Locate every Plasmodium falciparum-infected red blood cell.
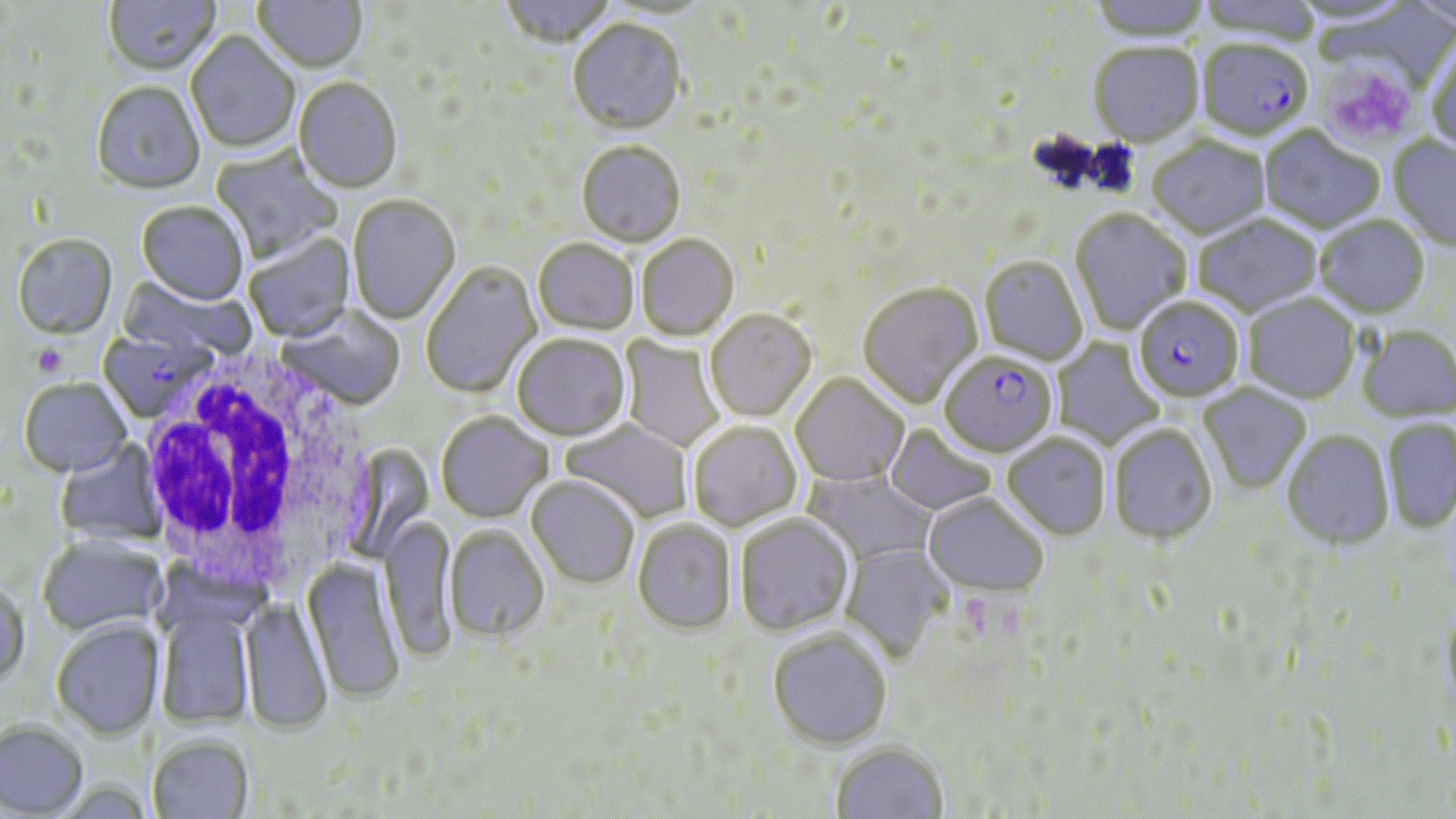

Approximate bounding boxes as [x1, y1, x2, y2] in pixels.
Plasmodium falciparum-infected red blood cells: [1196, 43, 1313, 145], [1133, 299, 1244, 405], [98, 329, 213, 423], [939, 354, 1057, 460].

White blood cell locations: [133, 354, 372, 595]. Platelet locations: [1324, 59, 1422, 158], [32, 346, 66, 377]. Uninfected red blood cell locations: [104, 0, 220, 78], [253, 0, 367, 75], [499, 0, 615, 51], [1086, 0, 1214, 44], [605, 2, 717, 22], [568, 21, 686, 137], [185, 32, 300, 155], [1425, 43, 1456, 157], [1088, 45, 1205, 149], [294, 78, 402, 195], [91, 83, 205, 198], [1259, 127, 1384, 235], [1387, 135, 1456, 254], [1148, 139, 1270, 241], [576, 143, 685, 249], [211, 145, 341, 263], [348, 197, 461, 326], [136, 204, 248, 307], [1069, 210, 1191, 334], [1194, 215, 1323, 319], [1314, 217, 1430, 321], [245, 232, 355, 343], [13, 236, 118, 342], [636, 236, 739, 343], [533, 241, 639, 337], [979, 258, 1088, 366], [422, 263, 542, 399], [118, 272, 255, 363], [858, 284, 983, 410], [1243, 295, 1360, 405], [278, 309, 405, 411], [705, 311, 816, 423], [1357, 327, 1456, 424], [619, 334, 726, 451], [512, 336, 630, 443], [1051, 337, 1164, 449], [791, 375, 909, 488], [19, 379, 132, 479], [1198, 383, 1311, 494], [436, 414, 553, 524], [561, 419, 693, 523], [1383, 419, 1456, 534], [688, 422, 803, 533], [884, 424, 997, 516], [1109, 426, 1217, 547], [1282, 431, 1394, 552], [1001, 434, 1111, 542], [56, 439, 168, 546], [801, 468, 938, 566], [526, 478, 639, 590], [922, 495, 1048, 600], [734, 515, 855, 638], [380, 518, 457, 665], [633, 521, 736, 636], [443, 528, 549, 645], [37, 536, 167, 637], [840, 543, 954, 664], [302, 559, 404, 705], [0, 578, 30, 688], [242, 599, 332, 737], [156, 602, 256, 729], [1441, 605, 1456, 720], [51, 620, 164, 741], [768, 632, 892, 752], [0, 720, 88, 817], [147, 736, 254, 819], [830, 744, 948, 818]. Slide-level diagnosis: Plasmodium falciparum. Light microscopy. Thin blood smear. Image is 1456×819 pixels. Single field of view. May-Grünwald-Giemsa-stained preparation. 1000x magnification.